Identify the parasite.
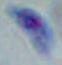
Toxoplasma gondii.

modality: photomicrograph
magnification: 1000x